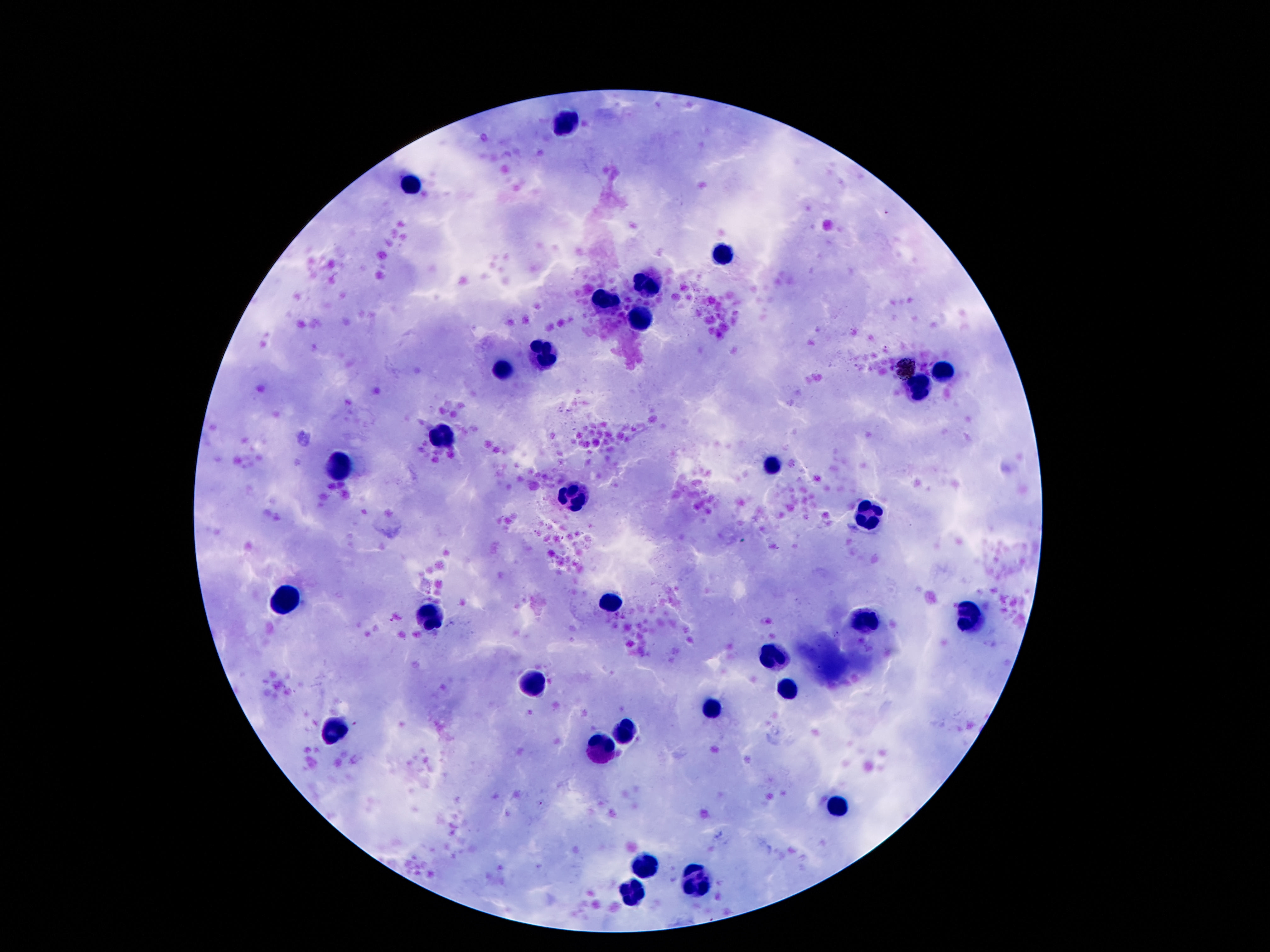
leukocyte locations = approximate object centers, in pixels from the top-left corner: (x=566, y=125), (x=414, y=185), (x=723, y=251), (x=650, y=282), (x=604, y=304), (x=638, y=319), (x=541, y=353), (x=503, y=369), (x=944, y=370), (x=919, y=389), (x=443, y=436), (x=774, y=463), (x=338, y=465), (x=571, y=497), (x=865, y=517), (x=289, y=599), (x=610, y=601), (x=429, y=615), (x=972, y=615), (x=867, y=620), (x=771, y=658), (x=534, y=685), (x=786, y=688), (x=709, y=708), (x=333, y=729), (x=625, y=732), (x=603, y=749), (x=841, y=809), (x=648, y=863), (x=697, y=880), (x=634, y=889)
stain = Giemsa
capture = smartphone camera through the microscope eyepiece
magnification = 100x
preparation = thick peripheral-blood smear
image size = 1270×952 pixels
patient malaria status = not infected
field of view = single